Report the malaria status of this cell.
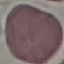

Uninfected.

Acquired by smartphone through the microscope eyepiece. Thin smear of blood. Automatically extracted cell patch, resized to 64 × 64 pixels. Giemsa-stained preparation.